Classify this cell by malaria status.
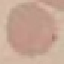
Uninfected.

Acquired by smartphone through the microscope eyepiece. Giemsa-stained preparation. Thin blood smear. Cell patch, automatically extracted from a larger field of view and resized to 64 × 64 pixels.